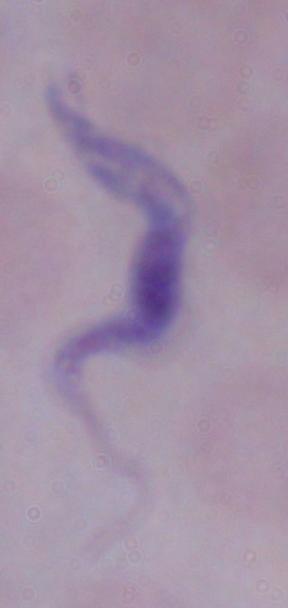
Summary:
  - Magnification: 1000x
  - Modality: micrograph
  - Identification: trypanosome